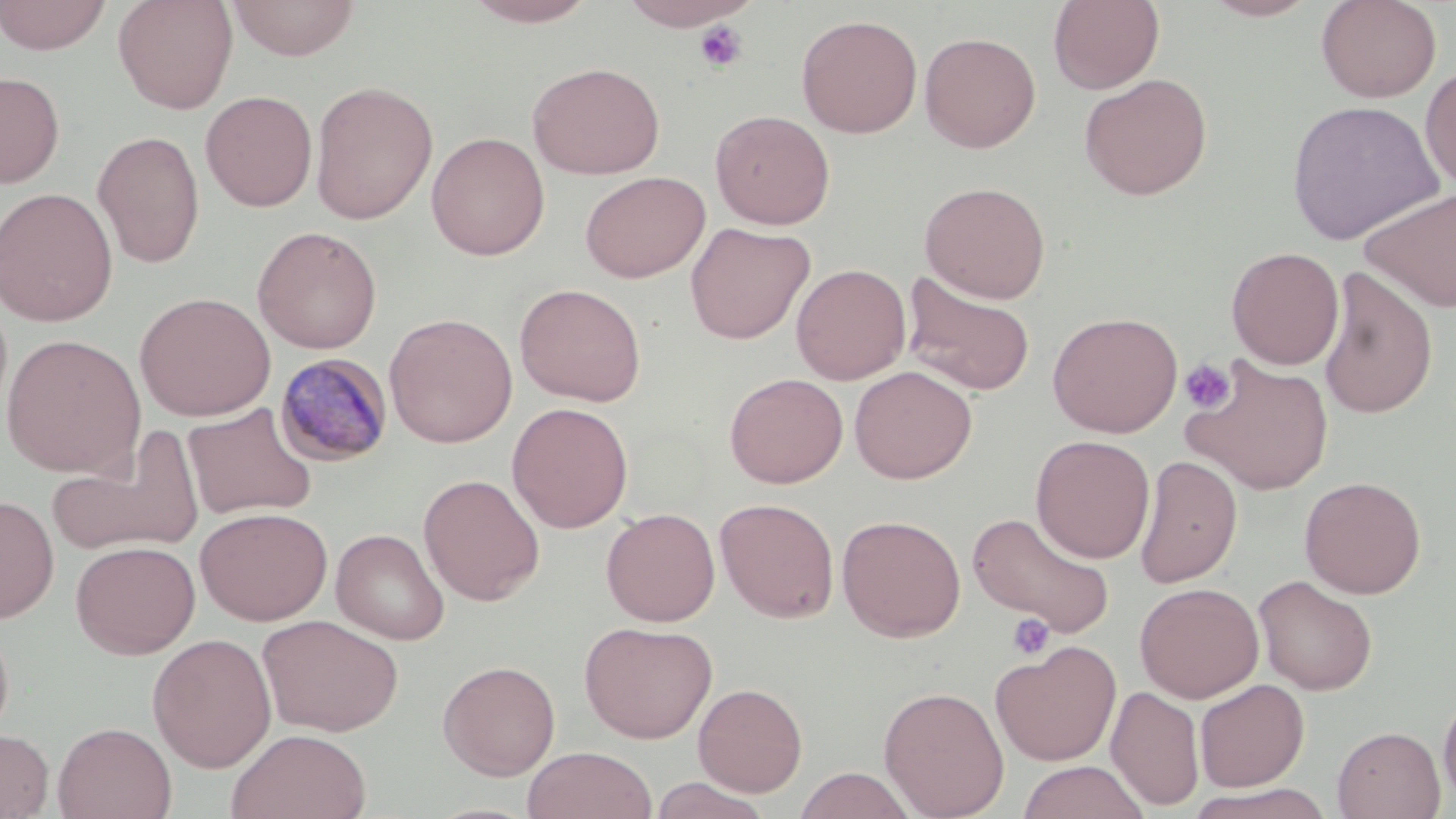
slide-level diagnosis = Plasmodium malariae
modality = light microscopy
uninfected red blood cell locations = approximate bounding boxes as named x1/y1/x2/y2 corners in pixels: (x1=0, y1=0, x2=112, y2=55), (x1=112, y1=0, x2=239, y2=114), (x1=227, y1=0, x2=360, y2=61), (x1=460, y1=0, x2=601, y2=27), (x1=617, y1=0, x2=761, y2=31), (x1=1048, y1=0, x2=1164, y2=94), (x1=1200, y1=0, x2=1322, y2=21), (x1=1316, y1=0, x2=1441, y2=102), (x1=796, y1=14, x2=923, y2=138), (x1=919, y1=31, x2=1041, y2=153), (x1=527, y1=61, x2=666, y2=179), (x1=1420, y1=65, x2=1456, y2=193), (x1=0, y1=71, x2=65, y2=189), (x1=1078, y1=73, x2=1213, y2=200), (x1=310, y1=81, x2=438, y2=225), (x1=200, y1=90, x2=318, y2=212), (x1=1285, y1=99, x2=1444, y2=245), (x1=710, y1=109, x2=835, y2=230), (x1=92, y1=129, x2=205, y2=269), (x1=426, y1=131, x2=550, y2=260), (x1=580, y1=170, x2=710, y2=283), (x1=919, y1=181, x2=1051, y2=303), (x1=1359, y1=186, x2=1456, y2=313), (x1=0, y1=187, x2=118, y2=327), (x1=685, y1=222, x2=815, y2=345), (x1=251, y1=225, x2=382, y2=354), (x1=1226, y1=246, x2=1345, y2=370), (x1=791, y1=263, x2=911, y2=385), (x1=1317, y1=267, x2=1438, y2=420), (x1=901, y1=270, x2=1037, y2=397), (x1=514, y1=282, x2=647, y2=407), (x1=134, y1=292, x2=276, y2=421), (x1=1046, y1=311, x2=1183, y2=438), (x1=383, y1=312, x2=518, y2=448), (x1=1, y1=333, x2=147, y2=478), (x1=1183, y1=356, x2=1334, y2=495), (x1=849, y1=365, x2=977, y2=484), (x1=724, y1=372, x2=848, y2=488), (x1=182, y1=402, x2=318, y2=521), (x1=506, y1=402, x2=633, y2=533), (x1=48, y1=427, x2=205, y2=559), (x1=1030, y1=435, x2=1155, y2=563), (x1=1135, y1=454, x2=1242, y2=589), (x1=418, y1=473, x2=545, y2=606), (x1=1299, y1=475, x2=1426, y2=599), (x1=0, y1=495, x2=59, y2=623), (x1=716, y1=498, x2=840, y2=623), (x1=195, y1=506, x2=332, y2=626), (x1=601, y1=507, x2=720, y2=627), (x1=967, y1=511, x2=1116, y2=639), (x1=837, y1=514, x2=966, y2=641), (x1=331, y1=528, x2=450, y2=645), (x1=70, y1=540, x2=200, y2=659), (x1=1254, y1=574, x2=1378, y2=695), (x1=1135, y1=582, x2=1264, y2=703), (x1=0, y1=615, x2=15, y2=748), (x1=257, y1=615, x2=404, y2=737), (x1=579, y1=620, x2=717, y2=744), (x1=147, y1=633, x2=277, y2=773), (x1=990, y1=640, x2=1122, y2=766), (x1=437, y1=660, x2=561, y2=780), (x1=1195, y1=678, x2=1310, y2=792), (x1=693, y1=682, x2=808, y2=796), (x1=878, y1=685, x2=1010, y2=818), (x1=1106, y1=685, x2=1205, y2=811), (x1=1438, y1=688, x2=1456, y2=809), (x1=52, y1=721, x2=177, y2=819), (x1=1332, y1=725, x2=1446, y2=819), (x1=226, y1=728, x2=372, y2=819), (x1=0, y1=729, x2=54, y2=818), (x1=522, y1=746, x2=658, y2=819), (x1=1016, y1=760, x2=1150, y2=819), (x1=793, y1=767, x2=918, y2=819), (x1=647, y1=775, x2=774, y2=819), (x1=1184, y1=784, x2=1339, y2=818)
platelet locations = approximate bounding boxes as named x1/y1/x2/y2 corners in pixels: (x1=694, y1=19, x2=747, y2=72), (x1=1179, y1=358, x2=1237, y2=413), (x1=1007, y1=613, x2=1055, y2=660)
magnification = 1000x
Plasmodium malariae-infected red blood cell locations = approximate bounding boxes as named x1/y1/x2/y2 corners in pixels: (x1=274, y1=352, x2=394, y2=467)
stain = May-Grünwald-Giemsa
field of view = single
image size = 1456×819 pixels
preparation = thin blood smear